Locate every blood parasite and identify its species.
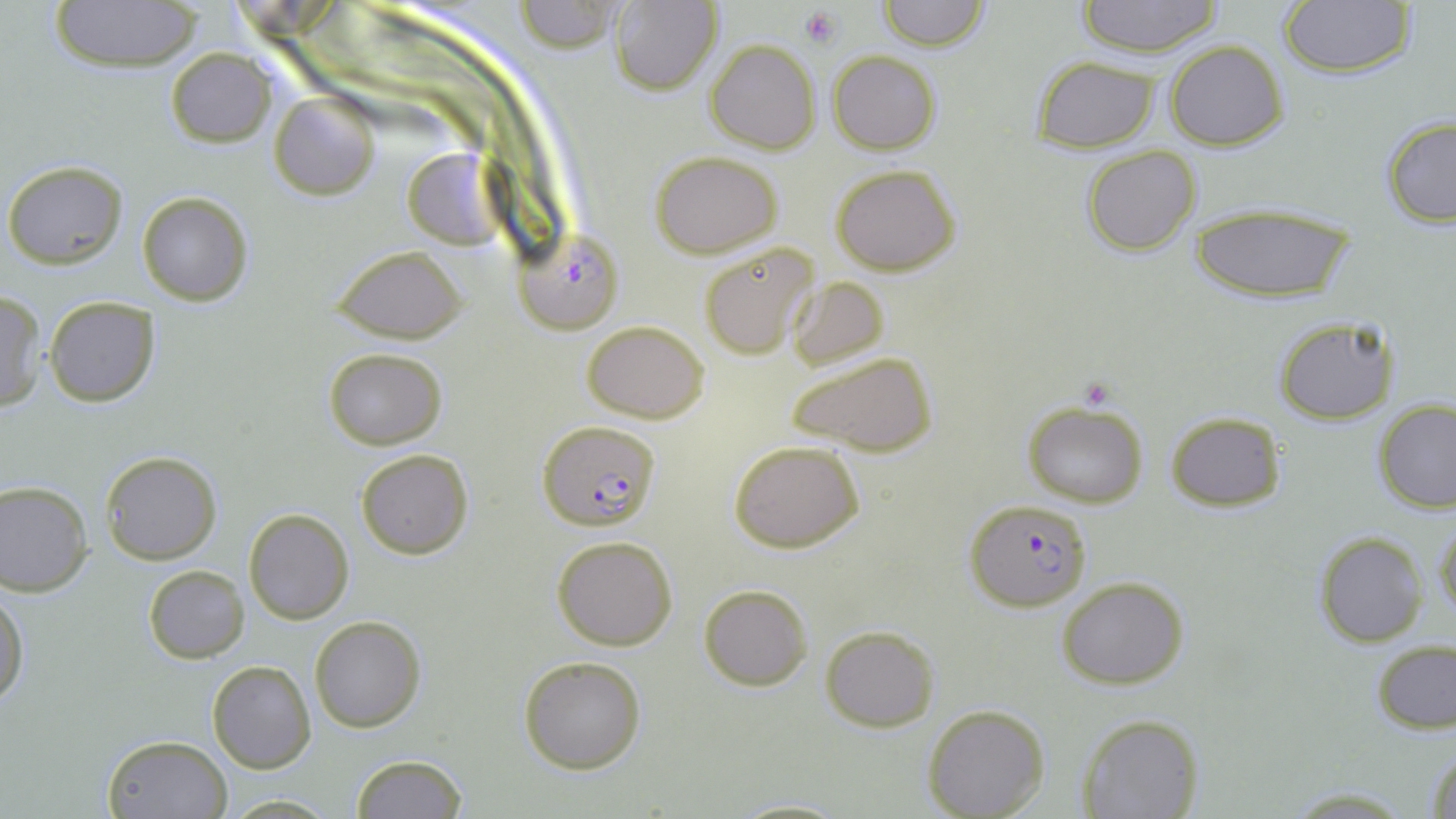

Approximate bounding boxes as (x1,y1)-(x2,y2) corner pairs in pixels.
Plasmodium falciparum-infected red blood cells: (513,233)-(622,335), (540,421)-(662,529), (964,497)-(1092,610).
No Plasmodium ovale, Plasmodium malariae, Plasmodium vivax, Babesia divergens, or Trypanosoma brucei observed.

slide-level diagnosis = Plasmodium falciparum
modality = light microscopy
image size = 1456×819 pixels
uninfected red blood cell locations = approximate bounding boxes as (x1,y1)-(x2,y2) corner pairs in pixels: (48,0)-(201,70), (878,0)-(989,50), (1077,0)-(1224,57), (514,1)-(623,53), (609,1)-(722,95), (1278,1)-(1416,77), (704,39)-(821,154), (1164,39)-(1287,151), (165,47)-(278,148), (827,50)-(940,153), (1031,56)-(1159,152), (269,90)-(379,200), (1380,113)-(1456,228), (1081,144)-(1202,255), (404,147)-(507,249), (649,149)-(783,258), (3,161)-(128,267), (831,164)-(960,275), (136,191)-(253,306), (1189,203)-(1358,303), (699,242)-(818,361), (333,246)-(467,344), (788,276)-(888,370), (1,290)-(46,412), (45,296)-(160,406), (1274,316)-(1397,424), (582,320)-(709,422), (324,347)-(448,450), (786,350)-(936,457), (1373,398)-(1456,513), (1022,401)-(1149,509), (1166,411)-(1286,510), (729,439)-(865,553), (355,448)-(473,559), (101,451)-(221,565), (0,480)-(94,596), (243,508)-(354,624), (1434,515)-(1456,626), (1314,533)-(1429,647), (551,534)-(678,651), (144,565)-(249,663), (1056,575)-(1190,690), (698,583)-(812,691), (0,587)-(27,708), (310,615)-(425,732), (821,625)-(939,730), (1372,640)-(1455,733), (518,654)-(646,773), (208,659)-(315,772), (923,703)-(1049,818), (1079,713)-(1204,818), (100,733)-(232,818), (1425,744)-(1456,819), (350,754)-(469,818), (1280,786)-(1417,817), (220,794)-(342,817), (731,798)-(850,818)
platelet locations = approximate bounding boxes as (x1,y1)-(x2,y2) corner pairs in pixels: (799,7)-(841,48)
field of view = one of a larger specimen
magnification = 1000x
stain = May-Grünwald-Giemsa
preparation = thin blood smear